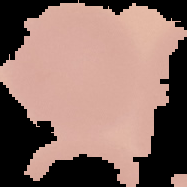
{
  "preparation": "thin blood smear",
  "malaria_status": "uninfected",
  "image_size": "187×187 pixels",
  "image_type": "cell region segmented out of the field of view; surrounding area masked to black"
}